Report the malaria status of this cell.
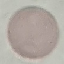

It is uninfected.

Thin blood film. Giemsa stain. Automatically extracted cell patch, resized to 64 × 64 pixels. Photographed with a smartphone camera at the microscope eyepiece.